Comment on the morphology of the red blood cells.
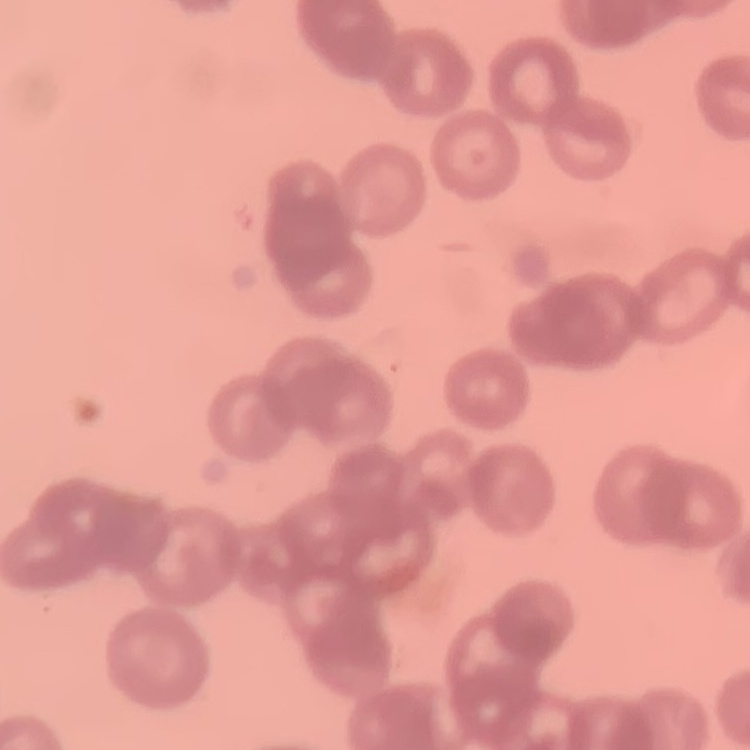
They show rouleaux formation.

preparation = thin blood film
stain = Field's or Giemsa
image type = one tile cut from a larger photomicrograph